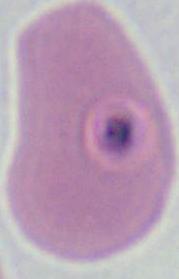

{
  "magnification": "400x or 1000x",
  "modality": "photomicrograph",
  "identification": "Plasmodium"
}